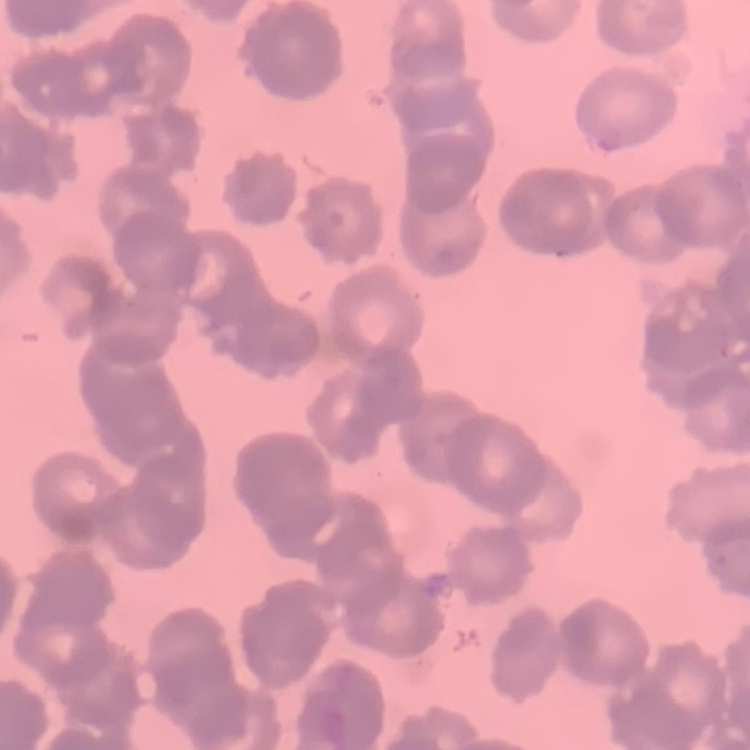

The erythrocytes exhibit rouleaux formation. Thin blood smear. Square crop of a larger photomicrograph. Field's or Giemsa stain.